Name the parasite shown.
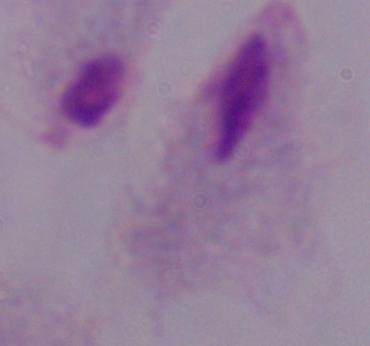

This is a trichomonad.

Captured at 1000x magnification. Photomicrograph.